Assess this cell for malaria.
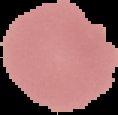
Uninfected.

Summary:
  - Preparation: thin blood film
  - Image size: 118×115 pixels
  - Image type: segmented cell region on a black background